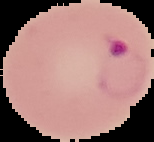

Summary:
  - Image size: 154×142 pixels
  - Image type: cell region segmented out of the field of view; surrounding area masked to black
  - Malaria status: parasitized
  - Preparation: thin blood film